Find the cells and give the type of each one.
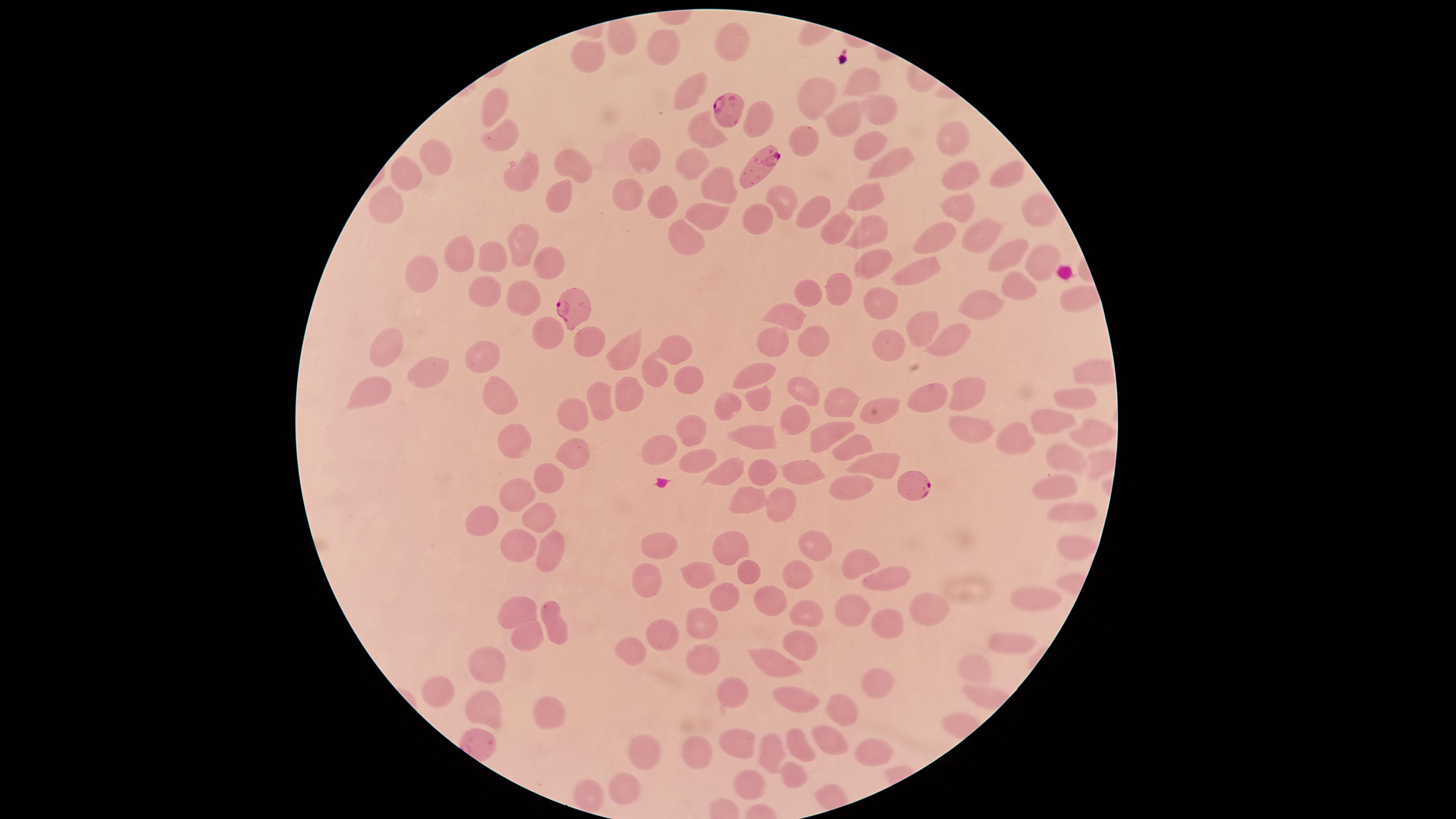

Approximate marker points as {x, y} in pixels.
Parasitized red blood cells: {733, 104}, {762, 164}, {580, 305}, {917, 484}.
Uninfected red blood cells: {620, 36}, {732, 37}, {664, 42}, {594, 53}, {858, 80}, {685, 89}, {820, 89}, {871, 103}, {494, 105}, {845, 117}, {753, 122}, {696, 133}, {500, 135}, {807, 141}, {863, 144}, {949, 144}, {640, 156}, {688, 156}, {437, 157}, {885, 158}, {573, 162}, {515, 165}, {409, 169}, {1006, 170}, {961, 173}, {716, 182}, {632, 191}, {547, 192}, {868, 196}, {781, 198}, {666, 199}, {388, 206}, {822, 207}, {964, 207}, {1036, 209}, {708, 212}, {758, 216}, {869, 228}, {845, 229}, {978, 232}, {938, 234}, {681, 235}, {529, 245}, {1002, 258}, {871, 259}, {1037, 259}, {462, 260}, {550, 260}, {493, 261}, {925, 271}, {431, 273}, {1019, 286}, {483, 287}, {846, 287}, {523, 292}, {810, 292}, {1078, 292}, {876, 298}, {984, 303}, {790, 311}, {923, 323}, {547, 331}, {592, 335}, {780, 335}, {960, 335}, {811, 338}, {675, 344}, {888, 345}, {624, 346}, {393, 348}, {476, 351}, {761, 370}, {432, 371}, {658, 372}, {1091, 374}, {692, 377}, {369, 385}, {503, 389}, {630, 391}, {805, 391}, {964, 391}, {605, 395}, {921, 395}, {1077, 395}, {758, 397}, {841, 398}, {729, 402}, {878, 405}, {568, 409}, {790, 421}, {1052, 421}, {689, 428}, {974, 428}, {831, 430}, {1089, 430}, {755, 435}, {1021, 436}, {513, 438}, {576, 447}, {855, 447}, {663, 449}, {1069, 455}, {698, 459}, {879, 463}, {729, 468}, {799, 469}, {763, 474}, {542, 478}, {843, 483}, {1050, 485}, {519, 491}, {776, 496}, {749, 497}, {1067, 513}, {536, 515}, {482, 517}, {520, 541}, {550, 544}, {657, 547}, {733, 547}, {1069, 547}, {817, 548}, {854, 567}, {743, 569}, {698, 572}, {793, 573}, {643, 575}, {882, 580}, {726, 591}, {770, 599}, {1032, 600}, {854, 604}, {937, 604}, {518, 608}, {808, 610}, {890, 618}, {697, 621}, {553, 625}, {661, 631}, {526, 633}, {1006, 636}, {632, 645}, {796, 651}, {765, 658}, {702, 659}, {492, 660}, {976, 669}, {880, 681}, {440, 690}, {740, 691}, {795, 698}, {840, 705}, {488, 707}, {546, 717}, {833, 736}, {739, 739}, {801, 743}, {866, 747}, {700, 750}, {770, 750}, {648, 752}, {793, 770}, {752, 780}, {630, 782}, {587, 793}.
No white blood cells identified.

Summary:
  - Visible region: circular
  - Field of view: single
  - Preparation: thin smear of blood
  - Image size: 1456×819 pixels
  - Species: Plasmodium falciparum
  - Stain: Giemsa
  - Capture: smartphone photograph through the microscope eyepiece